Describe the morphology of the red blood cells.
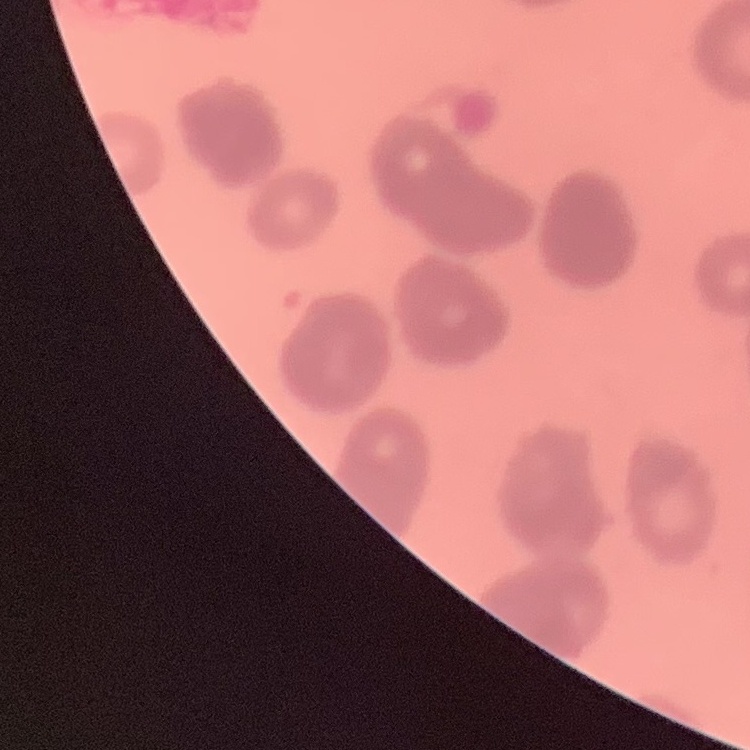
They show rouleaux formation.

Summary:
  - Preparation: thin blood smear
  - Image type: square crop of a larger photomicrograph
  - Stain: Field's or Giemsa